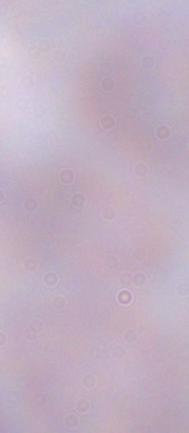

modality = micrograph
identification = trypanosome
magnification = 1000x